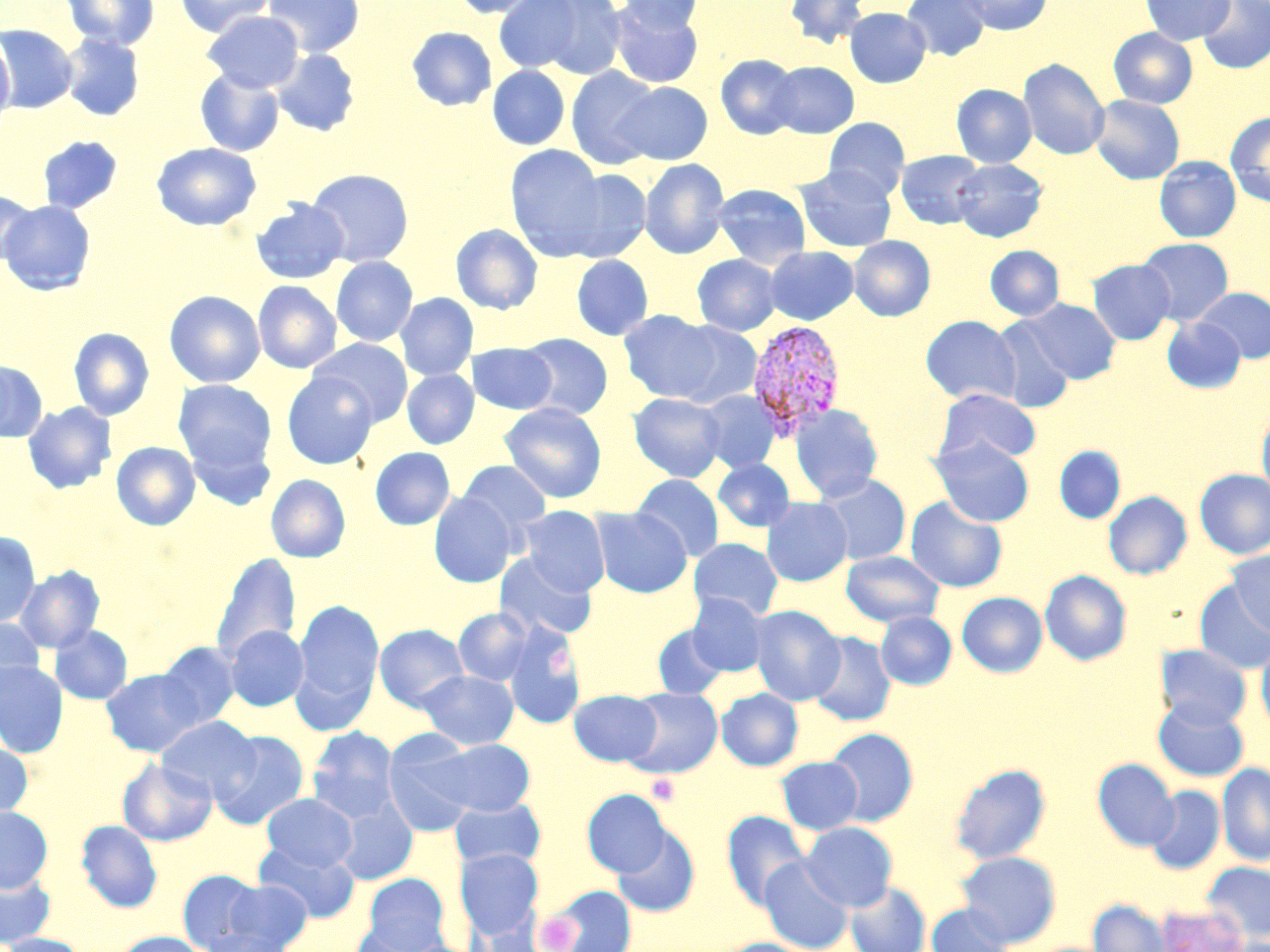

Approximate bounding boxes as (x1, y1, x2, y2) in pixels. Uninfected red blood cell locations: (61, 0, 159, 50), (174, 0, 275, 37), (263, 0, 364, 57), (449, 0, 545, 18), (492, 0, 588, 75), (528, 0, 629, 79), (618, 0, 705, 35), (785, 0, 871, 50), (901, 0, 990, 61), (959, 0, 1052, 35), (1140, 0, 1235, 45), (1197, 0, 1270, 73), (609, 3, 703, 88), (844, 7, 931, 87), (203, 10, 304, 93), (0, 25, 79, 114), (406, 26, 497, 111), (1108, 28, 1198, 108), (0, 32, 15, 125), (60, 33, 145, 121), (270, 49, 360, 137), (715, 54, 801, 139), (1019, 58, 1110, 160), (768, 61, 858, 138), (487, 65, 570, 150), (566, 66, 662, 170), (194, 68, 285, 156), (613, 81, 712, 165), (951, 84, 1037, 167), (1090, 94, 1185, 184), (1225, 111, 1270, 207), (822, 118, 911, 201), (37, 136, 123, 214), (151, 142, 261, 231), (504, 145, 608, 257), (896, 150, 987, 229), (1155, 156, 1241, 242), (639, 158, 731, 260), (950, 158, 1047, 242), (795, 165, 897, 252), (554, 168, 652, 262), (306, 169, 414, 267), (712, 184, 811, 269), (0, 190, 37, 266), (250, 198, 349, 285), (0, 200, 96, 295), (450, 223, 543, 315), (848, 235, 935, 321), (1137, 237, 1234, 325), (765, 245, 859, 325), (985, 245, 1064, 320), (692, 253, 782, 336), (571, 255, 653, 341), (331, 256, 418, 347), (1089, 259, 1175, 344), (253, 281, 342, 373), (1194, 287, 1270, 363), (164, 290, 265, 388), (395, 293, 479, 381), (1022, 298, 1121, 384), (618, 310, 727, 404), (920, 315, 1021, 405), (988, 317, 1076, 413), (1162, 317, 1246, 393), (657, 318, 763, 409), (69, 327, 154, 421), (518, 333, 613, 419), (309, 338, 413, 427), (468, 342, 557, 415), (0, 361, 47, 442), (402, 369, 478, 449), (281, 372, 379, 469), (173, 379, 277, 473), (935, 388, 1042, 464), (696, 390, 781, 473), (628, 392, 727, 482), (22, 402, 116, 494), (499, 402, 607, 503), (788, 403, 883, 502), (1257, 408, 1270, 500), (187, 436, 276, 512), (930, 437, 1034, 527), (111, 442, 200, 531), (1054, 446, 1125, 523), (370, 447, 455, 530), (713, 458, 796, 532), (458, 460, 552, 539), (1195, 469, 1270, 559), (631, 473, 725, 562), (813, 473, 911, 566), (265, 474, 351, 563), (1104, 491, 1192, 580), (429, 493, 517, 588), (905, 496, 1008, 592), (761, 497, 852, 587), (519, 506, 610, 595), (591, 507, 691, 597), (0, 532, 40, 628), (688, 537, 783, 621), (841, 551, 945, 627), (1226, 551, 1270, 636), (211, 552, 301, 664), (494, 552, 598, 641), (14, 565, 105, 653), (1040, 570, 1132, 666), (1194, 581, 1270, 673), (957, 592, 1047, 677), (688, 593, 769, 676), (293, 599, 384, 716), (750, 605, 845, 705), (453, 608, 534, 686), (876, 611, 956, 690), (0, 617, 45, 702), (374, 623, 470, 712), (502, 623, 584, 729), (50, 624, 133, 705), (652, 624, 729, 699), (225, 625, 309, 711), (808, 632, 896, 726), (156, 641, 243, 729), (1257, 641, 1270, 734), (1155, 644, 1252, 729), (0, 661, 68, 758), (100, 668, 206, 757), (417, 669, 519, 749), (620, 688, 723, 778), (717, 688, 803, 770), (569, 689, 661, 766), (1154, 699, 1249, 782), (156, 715, 260, 802), (307, 727, 399, 821), (824, 728, 919, 826), (209, 730, 309, 830), (382, 736, 480, 836), (427, 738, 536, 817), (0, 739, 33, 821), (775, 757, 863, 835), (118, 758, 217, 846), (1093, 758, 1179, 851), (1217, 762, 1270, 865), (950, 763, 1051, 864), (1146, 786, 1225, 874), (582, 789, 670, 877), (261, 793, 357, 871), (449, 796, 546, 871), (331, 798, 417, 885), (0, 806, 52, 891), (721, 811, 811, 912), (76, 820, 162, 913), (800, 822, 898, 911), (611, 825, 700, 918), (254, 841, 360, 922), (454, 848, 544, 939), (957, 851, 1061, 947), (759, 856, 854, 952), (1202, 862, 1270, 942), (0, 869, 56, 947), (177, 869, 265, 951), (363, 874, 449, 950), (223, 879, 313, 951), (845, 881, 931, 952), (545, 885, 637, 952), (1087, 899, 1171, 952), (926, 903, 1016, 952), (1156, 903, 1248, 952), (469, 918, 547, 952), (350, 922, 450, 952), (202, 929, 293, 952), (113, 932, 211, 952), (0, 933, 90, 952), (714, 938, 818, 952). Plasmodium vivax-infected red blood cell locations: (747, 319, 846, 440). Platelet locations: (546, 645, 574, 674), (647, 774, 681, 806), (535, 913, 580, 951). Slide-level diagnosis: Plasmodium vivax. Thin blood film. Optical microscopy. 1000x magnification. May-Grünwald-Giemsa-stained preparation. Image is 1270×952 pixels. One field of a larger specimen.